Assess this cell for malaria.
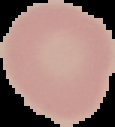

It is uninfected.

preparation = thin blood film
image size = 115×127 pixels
image type = segmented cell region on a black background